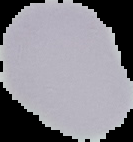
Summary:
  - Preparation: thin blood film
  - Malaria status: uninfected
  - Image size: 133×142 pixels
  - Image type: cell region segmented out of the field of view; surrounding area masked to black